Point out each leukocyte.
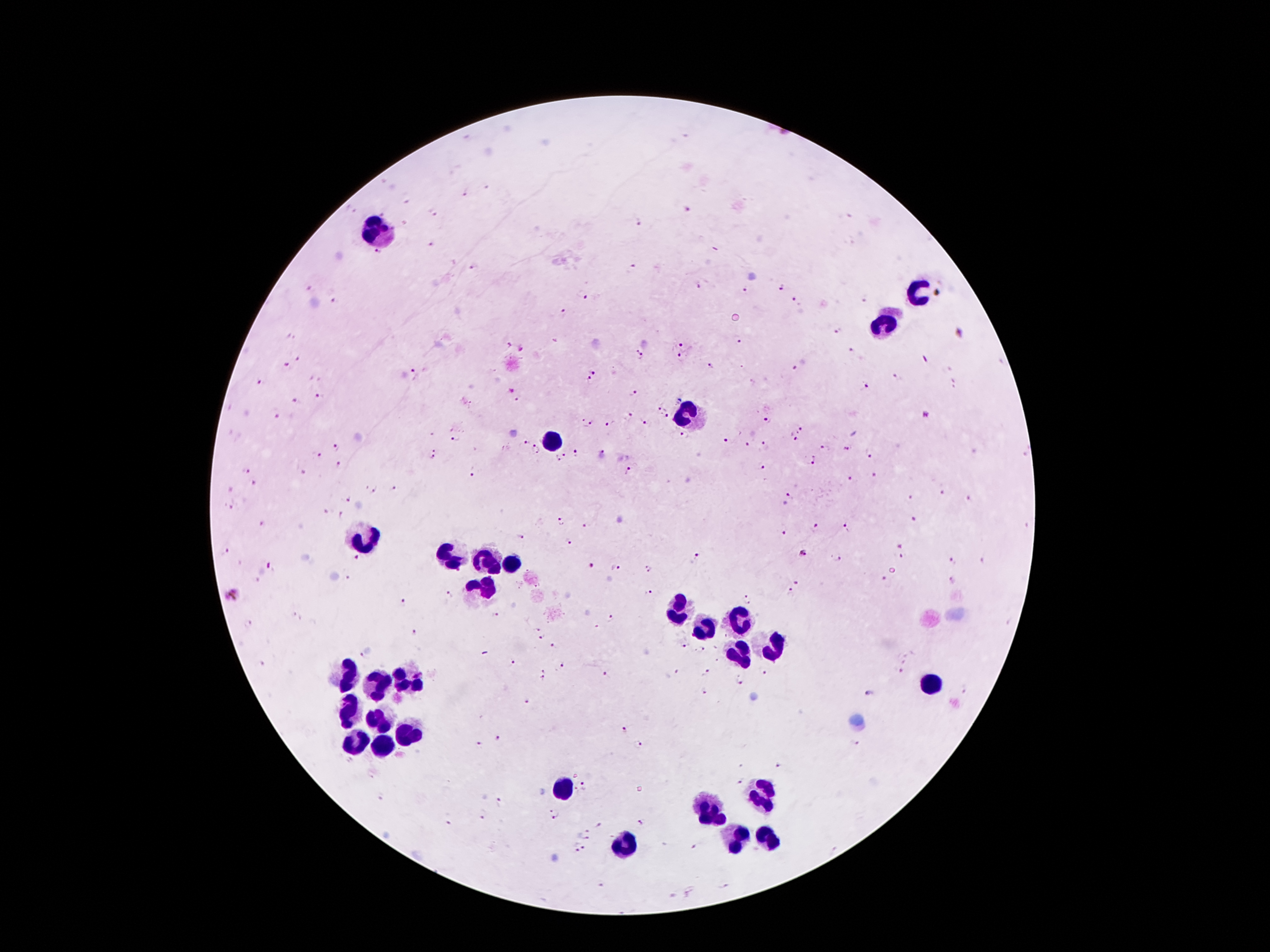

Approximate centers as (x, y) in pixels.
Leukocytes: (375, 230), (922, 291), (884, 324), (689, 412), (550, 444), (360, 539), (452, 558), (487, 562), (511, 562), (484, 585), (677, 610), (737, 620), (705, 631), (777, 647), (743, 655), (348, 673), (375, 681), (405, 681), (929, 682), (348, 713), (378, 720), (410, 732), (357, 741), (380, 747), (562, 786), (763, 794), (709, 813), (768, 835), (737, 839), (621, 844).

magnification: 100x
field_of_view: one from this slide
patient_malaria_status: infected with Plasmodium falciparum
plasmodium_parasite_locations: 'approximate centers as (x, y) in pixels: (486, 187), (466, 192), (407, 201), (688, 211), (351, 212), (433, 213), (640, 222), (431, 243), (377, 254), (471, 266), (633, 267), (699, 286), (782, 287), (308, 289), (745, 290), (583, 295), (867, 298), (797, 299), (333, 300), (564, 313), (839, 332), (960, 333), (291, 337), (738, 340), (681, 345), (521, 346), (854, 352), (641, 354), (298, 358), (681, 358), (284, 365), (710, 365), (794, 368), (595, 370), (415, 374), (898, 378), (590, 380), (260, 382), (955, 383), (863, 389), (511, 391), (632, 393), (321, 398), (298, 401), (660, 410), (277, 414), (926, 416), (628, 417), (666, 417), (767, 420), (645, 422), (586, 424), (610, 424), (799, 428), (685, 436), (454, 439), (725, 440), (794, 440), (523, 442), (746, 443), (336, 446), (764, 447), (826, 447), (847, 448), (537, 449), (575, 452), (871, 453), (316, 454), (433, 454), (564, 455), (602, 455), (557, 460), (814, 461), (337, 465), (764, 467), (246, 470), (474, 472), (629, 472), (303, 473), (874, 476), (850, 480), (256, 483), (395, 488), (376, 489), (943, 493), (790, 496), (912, 497), (346, 499), (969, 499), (229, 507), (326, 513), (341, 515), (914, 519), (560, 521), (262, 522), (586, 526), (816, 528), (845, 528), (785, 533), (520, 537), (570, 542), (898, 543), (225, 552), (904, 554), (806, 555), (838, 557), (356, 558), (694, 559), (983, 560), (953, 562), (270, 566), (589, 566), (616, 569), (649, 570), (350, 578), (883, 578), (796, 582), (953, 582), (451, 592), (648, 592), (788, 594), (233, 595), (750, 598), (403, 605), (297, 615), (497, 615), (613, 619), (248, 624), (536, 631), (415, 634), (542, 638), (555, 645), (681, 647), (703, 648), (362, 656), (510, 663), (261, 664), (564, 666), (545, 669), (676, 672), (902, 672), (708, 673), (764, 673), (606, 676), (542, 679), (740, 680), (965, 690), (703, 692), (869, 694), (526, 700), (625, 730), (498, 737), (855, 742), (480, 743), (639, 744), (743, 766), (777, 766), (741, 781), (585, 787), (381, 798), (500, 801), (554, 813), (483, 815), (446, 822), (639, 823), (598, 826), (588, 834), (694, 846), (581, 848), (601, 884)'
capture: smartphone through the microscope eyepiece
image_size: 1270×952 pixels
stain: Giemsa
preparation: thick blood film